Classify this cell by malaria status.
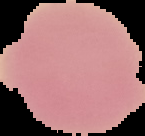
It is uninfected.

Summary:
  - Image type: segmented cell region with the area outside set to black
  - Preparation: thin blood smear
  - Image size: 145×136 pixels